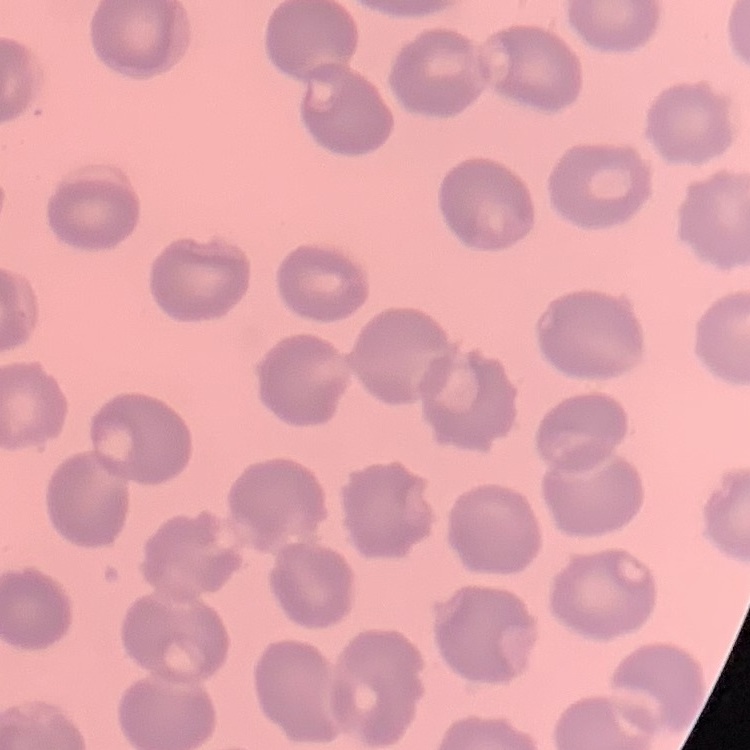

Summary:
  - Erythrocyte morphology: no rouleaux formation
  - Stain: Field's or Giemsa
  - Image type: square crop of a larger photomicrograph
  - Preparation: thin peripheral smear